Describe the morphology of the erythrocytes.
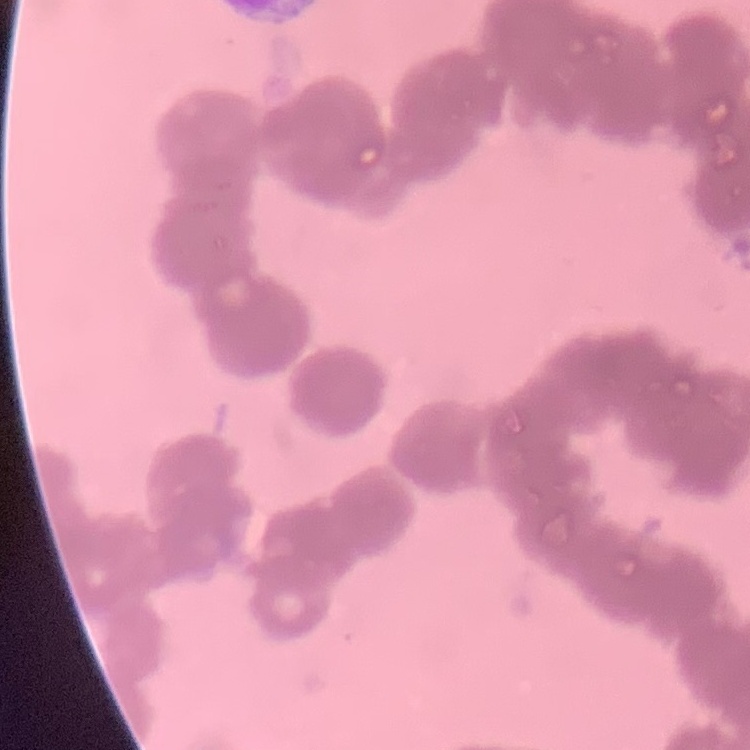

They show rouleaux formation.

Thin peripheral smear. Square crop of a larger photomicrograph. Field's or Giemsa stain.